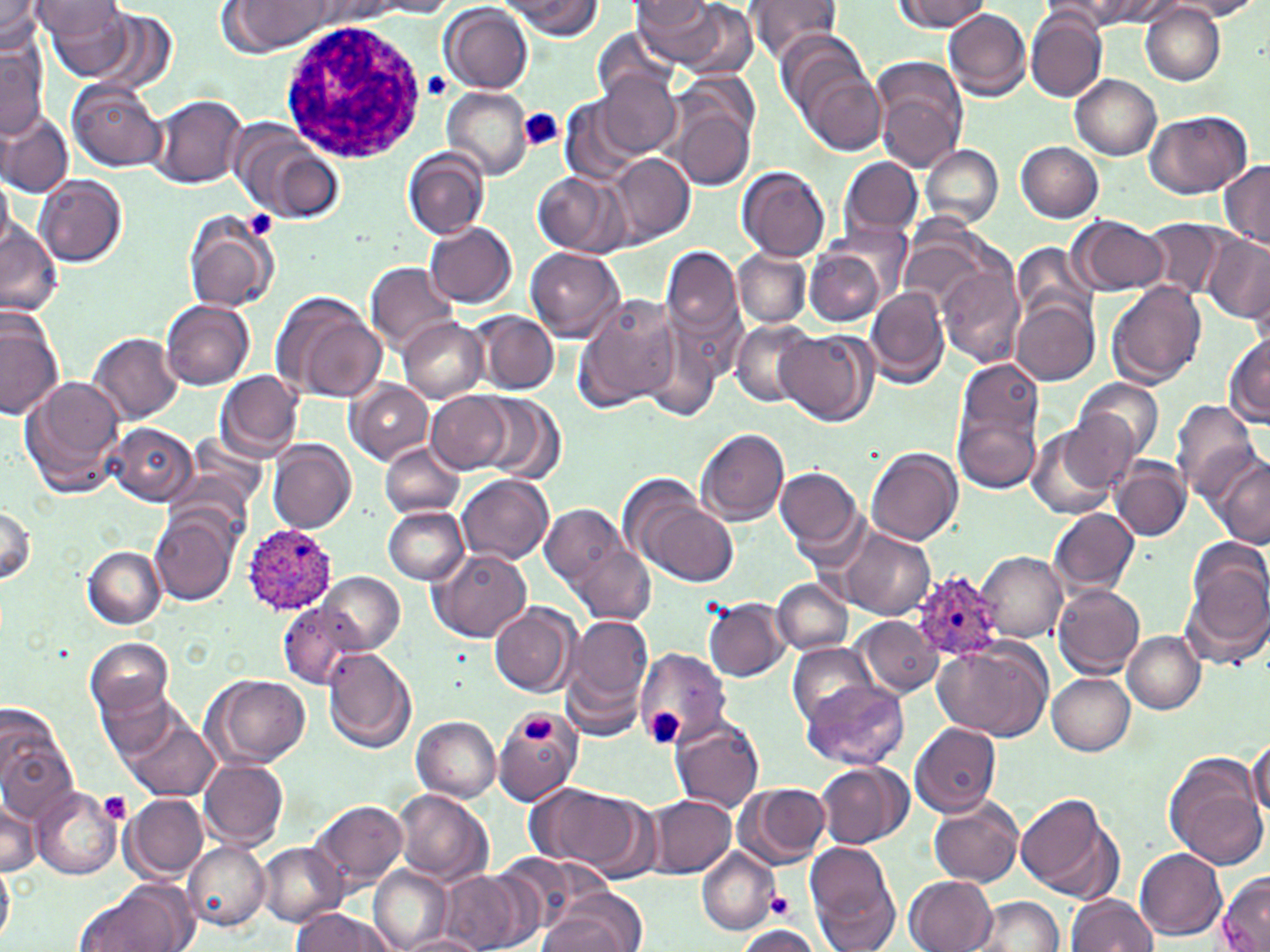

Approximate bounding boxes as (x1, y1, x2, y2) in pixels. White blood cell locations: (279, 16, 430, 164). Plasmodium ovale-infected red blood cell locations: (243, 523, 339, 614), (911, 570, 1006, 664). Platelet locations: (423, 71, 452, 98), (517, 110, 565, 153), (243, 212, 277, 241), (652, 710, 682, 745), (524, 716, 556, 743), (99, 791, 133, 823), (764, 892, 796, 920). Uninfected red blood cell locations: (0, 0, 45, 55), (33, 0, 135, 75), (505, 0, 603, 38), (742, 0, 844, 63), (892, 0, 991, 31), (1086, 0, 1187, 27), (1170, 0, 1266, 20), (224, 1, 334, 55), (364, 1, 458, 18), (631, 1, 743, 71), (1050, 1, 1152, 31), (1139, 2, 1224, 85), (632, 3, 716, 33), (441, 4, 533, 94), (83, 8, 180, 97), (944, 8, 1033, 101), (1025, 11, 1105, 102), (591, 29, 679, 104), (775, 29, 873, 122), (0, 39, 47, 138), (795, 56, 887, 155), (872, 58, 968, 172), (678, 69, 759, 146), (597, 72, 682, 157), (1070, 75, 1162, 161), (67, 80, 166, 172), (443, 86, 534, 180), (150, 93, 247, 188), (561, 99, 645, 186), (672, 107, 753, 189), (1145, 109, 1251, 199), (0, 111, 74, 198), (232, 123, 340, 220), (1017, 141, 1103, 222), (922, 144, 1003, 228), (403, 149, 488, 240), (610, 152, 694, 248), (840, 156, 924, 237), (1218, 159, 1270, 248), (738, 166, 830, 261), (533, 170, 623, 256), (0, 173, 15, 255), (35, 176, 127, 268), (183, 211, 280, 313), (1070, 217, 1168, 295), (1143, 218, 1231, 300), (425, 222, 518, 307), (0, 223, 63, 318), (827, 223, 911, 303), (901, 228, 998, 311), (1201, 232, 1270, 323), (1010, 242, 1098, 327), (662, 243, 745, 350), (806, 245, 890, 328), (525, 247, 625, 342), (733, 248, 812, 328), (365, 262, 459, 353), (937, 263, 1023, 369), (1106, 281, 1206, 388), (866, 285, 950, 389), (271, 291, 385, 403), (573, 293, 682, 412), (161, 299, 256, 390), (1012, 299, 1098, 386), (0, 308, 64, 421), (476, 312, 559, 394), (397, 317, 487, 402), (729, 320, 816, 407), (639, 325, 726, 423), (775, 329, 878, 427), (89, 331, 183, 423), (1224, 333, 1270, 428), (956, 356, 1044, 455), (216, 370, 304, 461), (20, 376, 126, 498), (1074, 377, 1165, 464), (347, 380, 433, 465), (427, 392, 511, 472), (479, 392, 564, 484), (1171, 401, 1259, 500), (954, 407, 1039, 492), (1053, 411, 1138, 496), (106, 422, 198, 506), (1025, 424, 1123, 519), (696, 429, 790, 524), (267, 439, 356, 534), (378, 442, 465, 520), (866, 447, 962, 545), (1111, 456, 1191, 541), (1211, 456, 1269, 546), (776, 466, 864, 557), (456, 474, 553, 565), (633, 491, 740, 587), (1, 502, 37, 587), (539, 503, 635, 602), (381, 505, 469, 584), (1049, 507, 1139, 595), (151, 512, 240, 605), (833, 525, 936, 621), (573, 545, 656, 625), (83, 546, 165, 627), (1188, 547, 1269, 646), (430, 548, 531, 642), (977, 552, 1067, 641), (319, 572, 403, 653), (772, 579, 852, 655), (1053, 583, 1146, 678), (1180, 587, 1265, 673), (703, 597, 789, 681), (278, 601, 361, 689), (489, 603, 578, 697), (561, 612, 657, 726), (855, 616, 943, 696), (1122, 631, 1205, 714), (86, 637, 176, 722), (934, 641, 1054, 740), (787, 642, 878, 727), (323, 646, 416, 753), (634, 647, 732, 748), (1046, 672, 1135, 754), (207, 673, 311, 768), (92, 677, 183, 763), (801, 680, 910, 769), (492, 711, 581, 805), (411, 715, 500, 802), (123, 716, 219, 802), (671, 717, 766, 813), (910, 723, 1002, 817), (0, 730, 79, 825), (1247, 741, 1269, 821), (1163, 754, 1269, 871), (200, 758, 289, 848), (816, 761, 913, 849), (733, 781, 831, 870), (531, 784, 649, 875), (30, 787, 122, 880), (394, 789, 493, 884), (1016, 791, 1121, 901), (123, 792, 210, 882), (646, 794, 737, 878), (1, 795, 40, 876), (929, 796, 1025, 889), (313, 798, 409, 893), (182, 841, 270, 930), (257, 842, 346, 925), (805, 844, 899, 950), (697, 849, 778, 935), (1136, 850, 1227, 941), (491, 854, 590, 935), (0, 860, 15, 943), (369, 865, 452, 951), (440, 871, 529, 952), (1215, 871, 1270, 952), (905, 875, 996, 952), (78, 881, 199, 952), (1065, 894, 1157, 951), (970, 895, 1064, 951), (542, 896, 642, 952), (291, 909, 391, 951), (733, 925, 826, 951), (395, 933, 486, 952). Slide-level diagnosis: Plasmodium ovale. One field of a larger specimen. Thin blood film. Image is 1270×952 pixels. May-Grünwald-Giemsa-stained preparation. 1000x magnification. Light microscopy.